Report the malaria status of this cell.
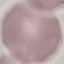

It is uninfected.

{
  "image_type": "cell patch, automatically extracted from a larger field of view and resized to 64 × 64 pixels",
  "stain": "Giemsa",
  "preparation": "thin smear",
  "capture": "smartphone through the microscope eyepiece"
}